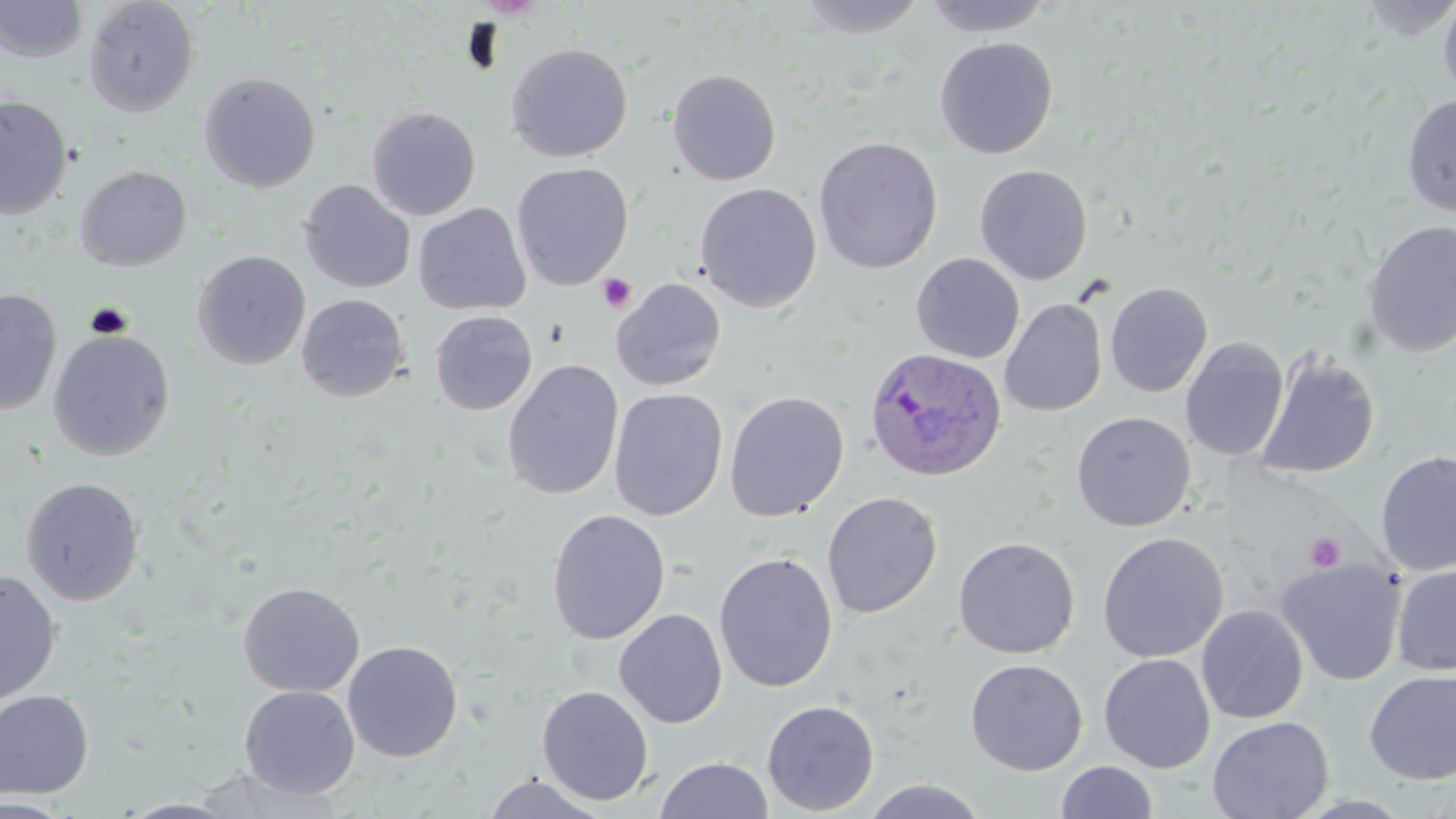

slide-level diagnosis = Plasmodium ovale
magnification = 1000x
field of view = single
image size = 1456×819 pixels
Plasmodium ovale-infected red blood cell locations = approximate bounding boxes as [x1, y1, x2, y2] in pixels: [864, 348, 1007, 483]
platelet locations = approximate bounding boxes as [x1, y1, x2, y2] in pixels: [599, 273, 637, 312], [1305, 532, 1345, 572]
uninfected red blood cell locations = approximate bounding boxes as [x1, y1, x2, y2] in pixels: [2, 0, 147, 90], [83, 0, 199, 116], [793, 0, 931, 38], [919, 0, 1056, 36], [1356, 0, 1456, 41], [1438, 0, 1456, 102], [1, 1, 88, 63], [934, 37, 1059, 158], [505, 43, 633, 162], [666, 69, 782, 186], [199, 72, 321, 193], [1402, 94, 1456, 217], [0, 95, 73, 219], [366, 106, 481, 219], [813, 136, 943, 273], [511, 162, 633, 290], [974, 164, 1093, 285], [75, 165, 192, 271], [299, 180, 416, 294], [695, 183, 822, 312], [413, 203, 532, 316], [1363, 220, 1456, 357], [192, 250, 310, 370], [911, 253, 1025, 364], [610, 278, 727, 391], [1104, 281, 1213, 397], [0, 287, 62, 415], [296, 294, 409, 402], [1000, 299, 1107, 417], [429, 310, 537, 415], [48, 330, 175, 461], [1180, 337, 1288, 461], [1256, 351, 1381, 480], [503, 359, 624, 500], [609, 388, 728, 521], [724, 390, 849, 522], [1071, 411, 1196, 532], [1375, 450, 1456, 576], [20, 477, 145, 606], [822, 491, 943, 619], [546, 508, 671, 645], [1096, 532, 1229, 663], [953, 536, 1080, 659], [714, 552, 838, 693], [1275, 558, 1406, 686], [1391, 563, 1456, 676], [0, 570, 61, 706], [238, 582, 365, 698], [1196, 605, 1308, 724], [614, 609, 728, 729], [342, 640, 463, 762], [1098, 653, 1215, 773], [964, 658, 1088, 775], [1364, 669, 1456, 785], [239, 685, 360, 798], [536, 685, 654, 806], [0, 689, 94, 799], [761, 699, 880, 816], [1207, 715, 1334, 819], [655, 756, 774, 818], [1055, 761, 1159, 819], [187, 769, 346, 817], [479, 774, 612, 818], [860, 779, 991, 819], [0, 797, 77, 818], [117, 798, 244, 818]
stain = May-Grünwald-Giemsa
modality = light microscopy
preparation = thin blood film